Locate every Plasmodium ovale-infected red blood cell.
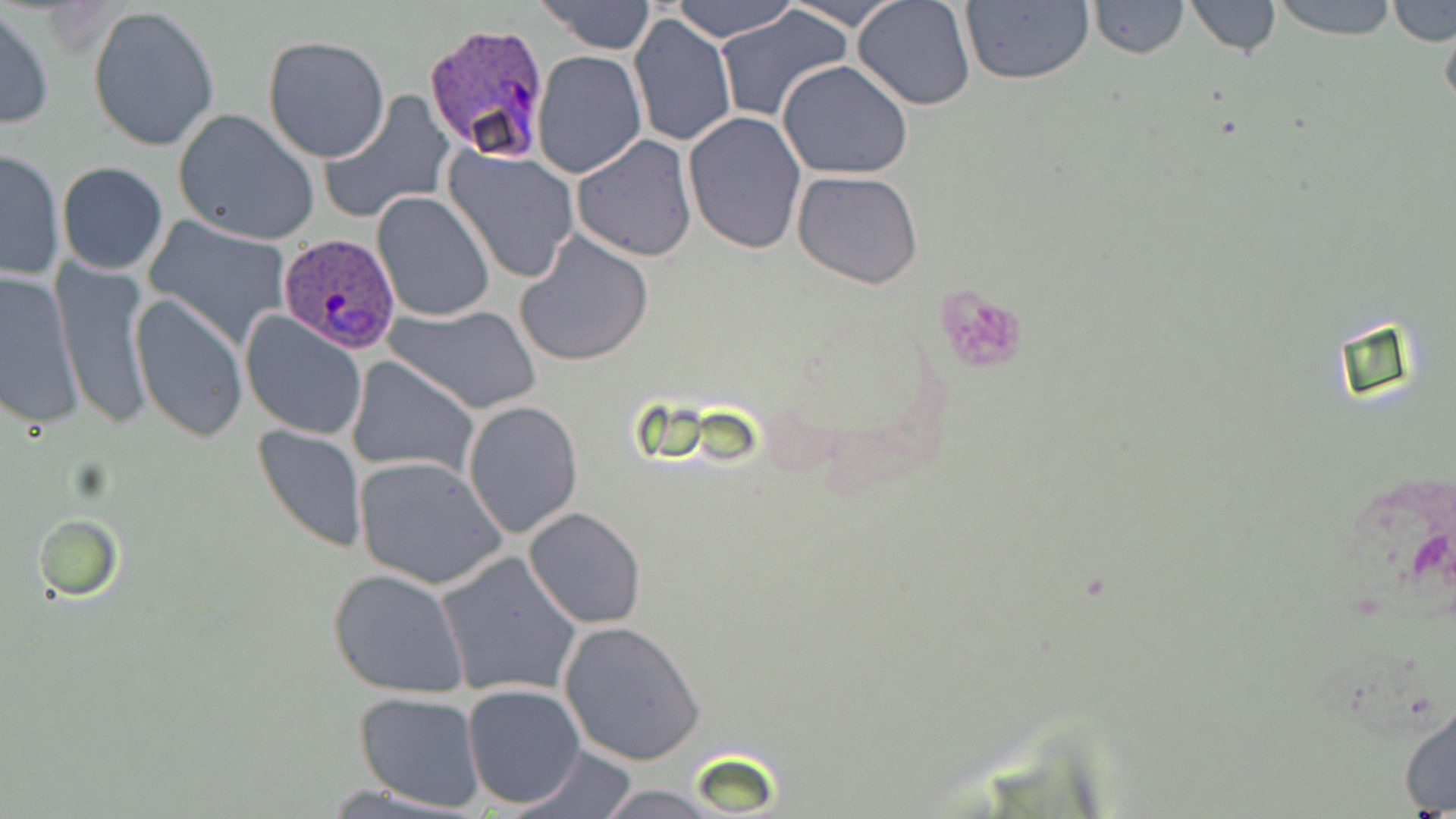

Approximate bounding boxes as named x1/y1/x2/y2 corners in pixels.
Plasmodium ovale-infected red blood cells: (x1=424, y1=21, x2=549, y2=163), (x1=278, y1=234, x2=399, y2=353).

slide-level diagnosis = Plasmodium ovale
preparation = thin blood film
uninfected red blood cell locations = approximate bounding boxes as named x1/y1/x2/y2 corners in pixels: (x1=538, y1=0, x2=656, y2=52), (x1=671, y1=0, x2=797, y2=43), (x1=784, y1=0, x2=905, y2=30), (x1=852, y1=0, x2=978, y2=111), (x1=960, y1=0, x2=1096, y2=86), (x1=1087, y1=0, x2=1189, y2=60), (x1=1184, y1=0, x2=1283, y2=57), (x1=1266, y1=0, x2=1401, y2=39), (x1=1387, y1=0, x2=1455, y2=47), (x1=0, y1=5, x2=53, y2=130), (x1=88, y1=6, x2=220, y2=152), (x1=715, y1=6, x2=849, y2=124), (x1=1441, y1=10, x2=1456, y2=119), (x1=628, y1=11, x2=737, y2=149), (x1=263, y1=35, x2=390, y2=161), (x1=532, y1=49, x2=647, y2=177), (x1=776, y1=60, x2=914, y2=180), (x1=318, y1=91, x2=454, y2=223), (x1=172, y1=109, x2=319, y2=245), (x1=683, y1=111, x2=809, y2=253), (x1=571, y1=134, x2=698, y2=261), (x1=1, y1=147, x2=66, y2=282), (x1=445, y1=148, x2=580, y2=281), (x1=57, y1=162, x2=169, y2=276), (x1=792, y1=170, x2=924, y2=288), (x1=370, y1=191, x2=495, y2=323), (x1=145, y1=216, x2=295, y2=349), (x1=514, y1=233, x2=653, y2=368), (x1=52, y1=260, x2=156, y2=430), (x1=0, y1=268, x2=84, y2=428), (x1=131, y1=292, x2=248, y2=442), (x1=386, y1=302, x2=541, y2=416), (x1=240, y1=310, x2=368, y2=440), (x1=346, y1=356, x2=480, y2=478), (x1=463, y1=400, x2=583, y2=539), (x1=253, y1=423, x2=367, y2=551), (x1=352, y1=455, x2=504, y2=592), (x1=523, y1=507, x2=646, y2=629), (x1=34, y1=514, x2=124, y2=601), (x1=435, y1=550, x2=582, y2=696), (x1=328, y1=568, x2=472, y2=699), (x1=559, y1=620, x2=706, y2=764), (x1=463, y1=684, x2=584, y2=808), (x1=353, y1=691, x2=485, y2=812), (x1=1399, y1=702, x2=1456, y2=814), (x1=503, y1=746, x2=641, y2=817), (x1=583, y1=782, x2=736, y2=819)
stain = May-Grünwald-Giemsa
magnification = 1000x
field of view = single
image size = 1456×819 pixels
modality = optical microscopy
platelet locations = approximate bounding boxes as named x1/y1/x2/y2 corners in pixels: (x1=937, y1=287, x2=1027, y2=374)